Classify this cell by malaria status.
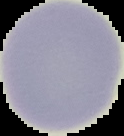
It is uninfected.

Summary:
  - Image size: 124×136 pixels
  - Image type: segmented cell region on a black background
  - Preparation: thin blood smear